Give the position of every Plasmodium parasite visible.
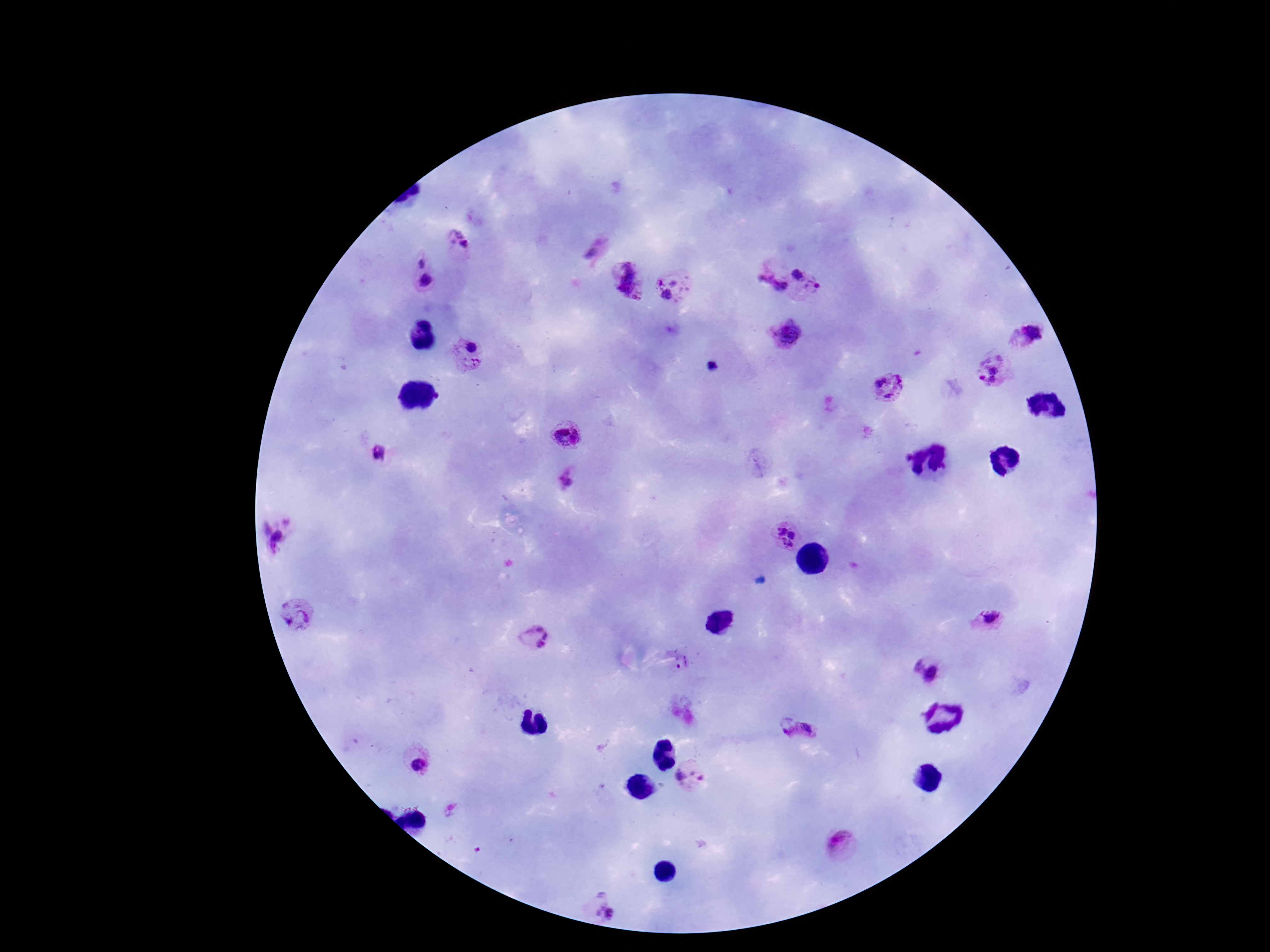
Approximate centers as {x, y} in pixels.
Plasmodium parasites: {459, 245}, {593, 247}, {422, 275}, {624, 275}, {807, 282}, {769, 284}, {669, 287}, {1030, 331}, {790, 335}, {470, 354}, {996, 366}, {713, 367}, {889, 386}, {568, 434}, {378, 453}, {568, 477}, {278, 534}, {787, 537}, {298, 615}, {987, 619}, {534, 637}, {930, 669}, {801, 734}, {419, 762}, {695, 777}, {842, 844}, {604, 905}.

Summary:
  - Image size: 1270×952 pixels
  - Capture: smartphone camera through the microscope eyepiece
  - Preparation: thick peripheral-blood smear
  - Stain: Giemsa
  - Magnification: 100x
  - Field of view: single
  - Patient malaria status: infected